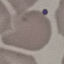
result = no malaria parasites seen
stain = Giemsa
preparation = thin blood smear
image type = cell patch, automatically extracted from a larger field of view and resized to 64 × 64 pixels
capture = smartphone through the microscope eyepiece